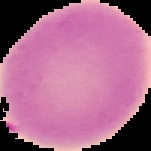

Summary:
  - Image size: 151×151 pixels
  - Malaria status: uninfected
  - Image type: segmented cell region on a black background
  - Preparation: thin blood smear